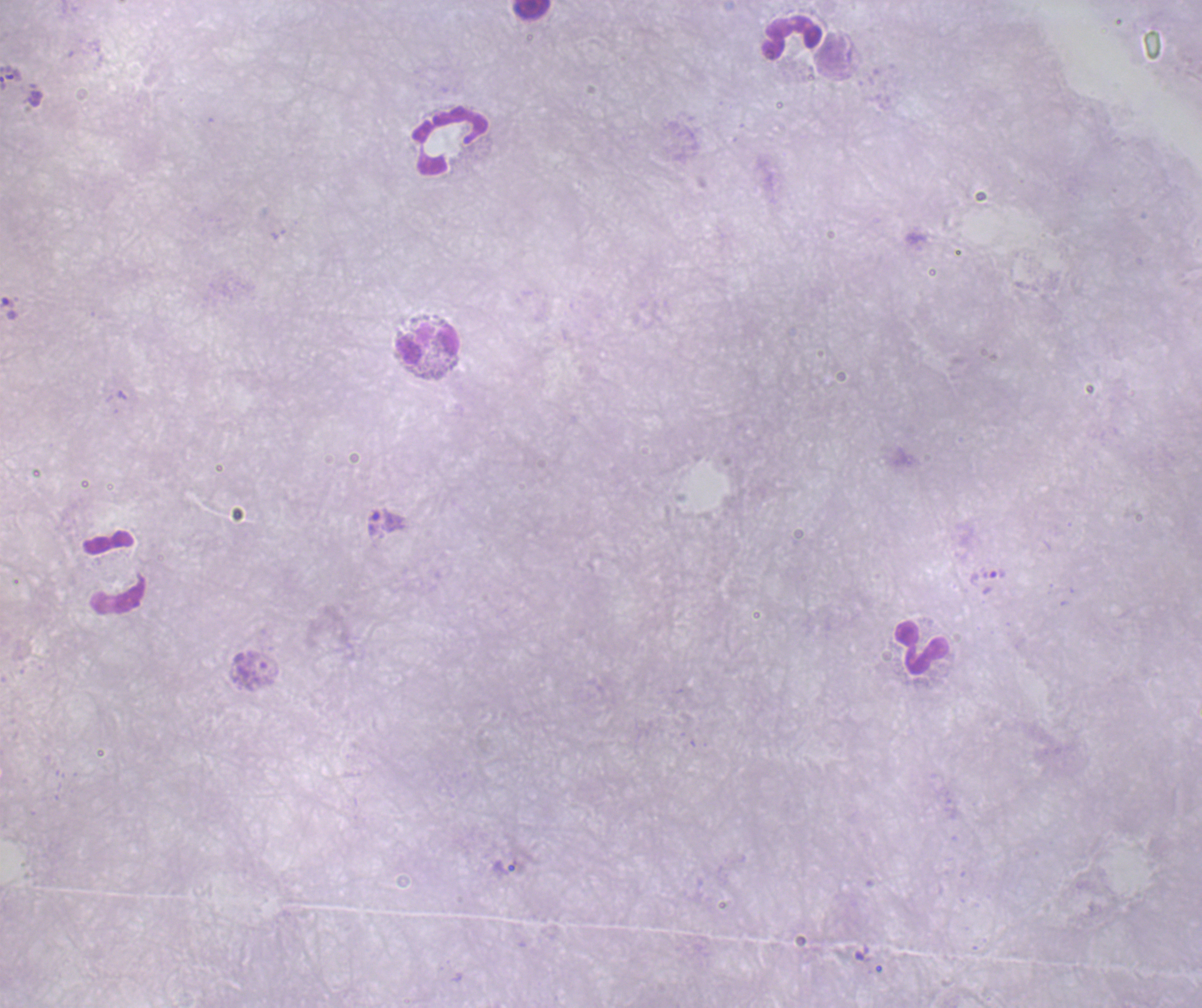

Approximate centers as (x, y) in pixels. Leukocyte locations: (531, 10), (791, 37), (450, 140), (429, 346), (114, 574), (921, 647). Trophozoite locations: (386, 520), (994, 573), (506, 867). Result: malaria parasites identified. Background quality: poor. Image is 1202×1008 pixels. Previously used in a real diagnosis. 100x magnification. Single field of view. Romanowsky-stained preparation. Coloration quality: bad. Thick blood film.